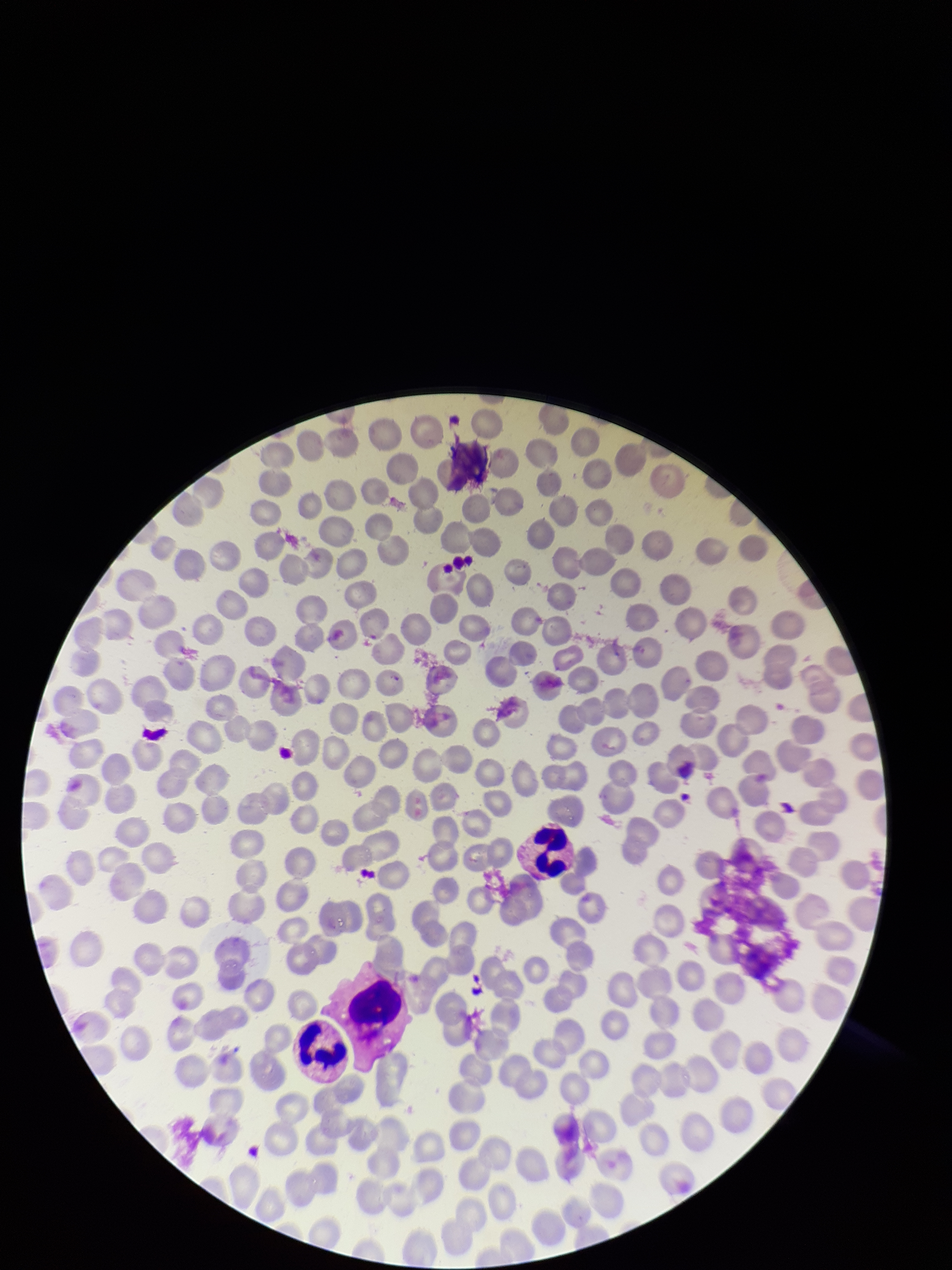
{
  "field_of_view": "single",
  "stain": "Giemsa",
  "parasitized_red_blood_cell_count": 0,
  "preparation": "thin",
  "red_blood_cell_count": 224,
  "patient_malaria_status": "negative",
  "image_size": "952×1270 pixels",
  "parasitized_red_blood_cells": "none detected",
  "capture": "smartphone photograph through the microscope eyepiece"
}